Describe the morphology of the erythrocytes.
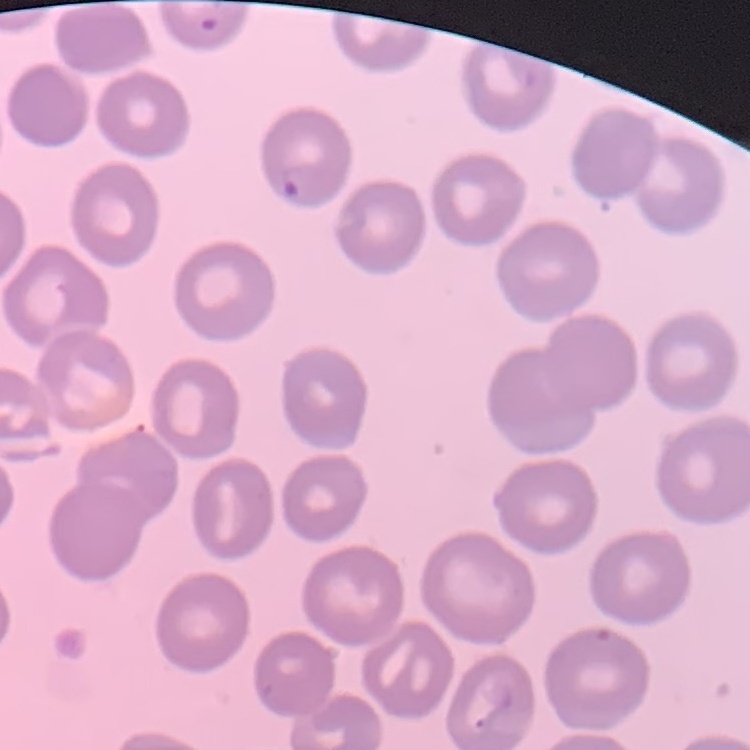
No rouleaux formation.

Field's or Giemsa stain. Square crop of a larger photomicrograph. Thin peripheral smear.